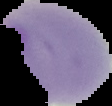

image size = 112×106 pixels
result = no Plasmodium parasites detected
preparation = thin blood smear
image type = segmented cell region with the area outside set to black